Describe the morphology of the erythrocytes.
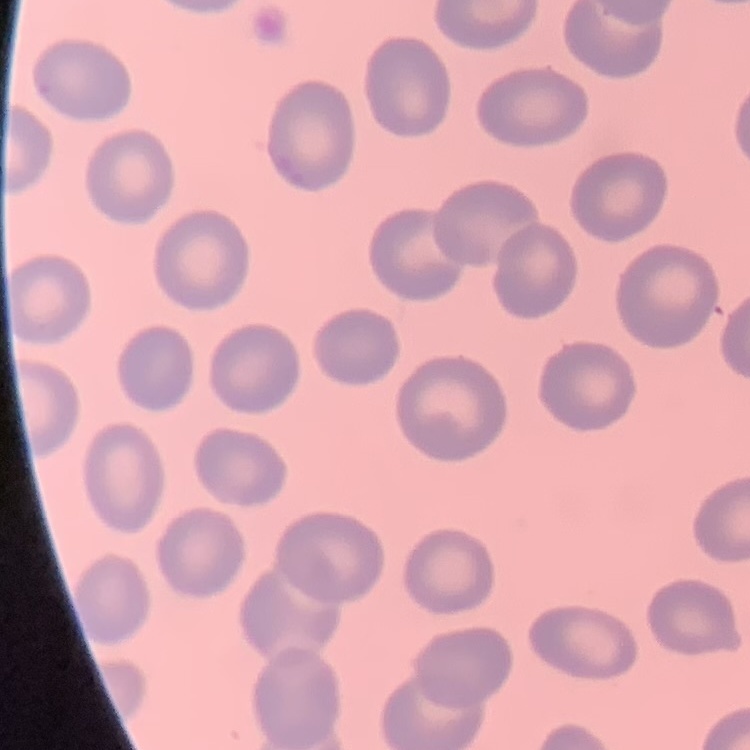
No rouleaux formation.

Summary:
  - Preparation: thin peripheral smear
  - Stain: Field's or Giemsa
  - Image type: one tile cut from a larger photomicrograph